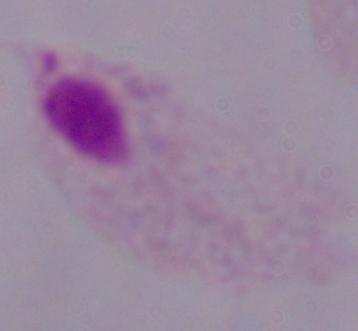 Photomicrograph. Captured at 1000x magnification. A trichomonad is shown.